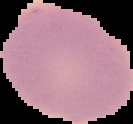

Image is 133×124 pixels. Malaria status: uninfected. The area outside the segmented cell region is set to black. From a thin blood smear.